Comment on the morphology of the red blood cells.
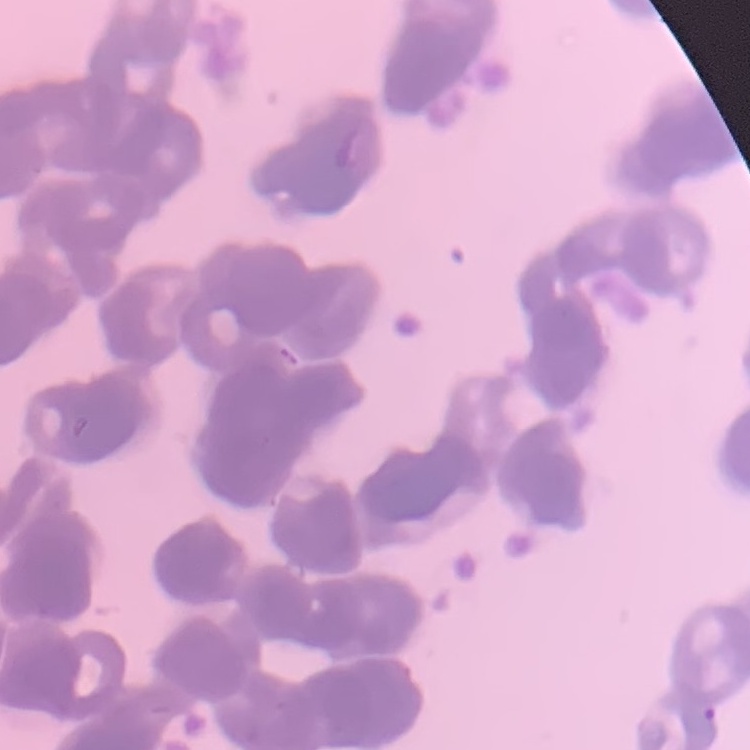
They show rouleaux formation.

Field's or Giemsa stain. Square crop of a larger photomicrograph. Thin peripheral smear.